Give the position of every malaria parasite, noting whether each is a trophozoite, schizont, or gametocyte.
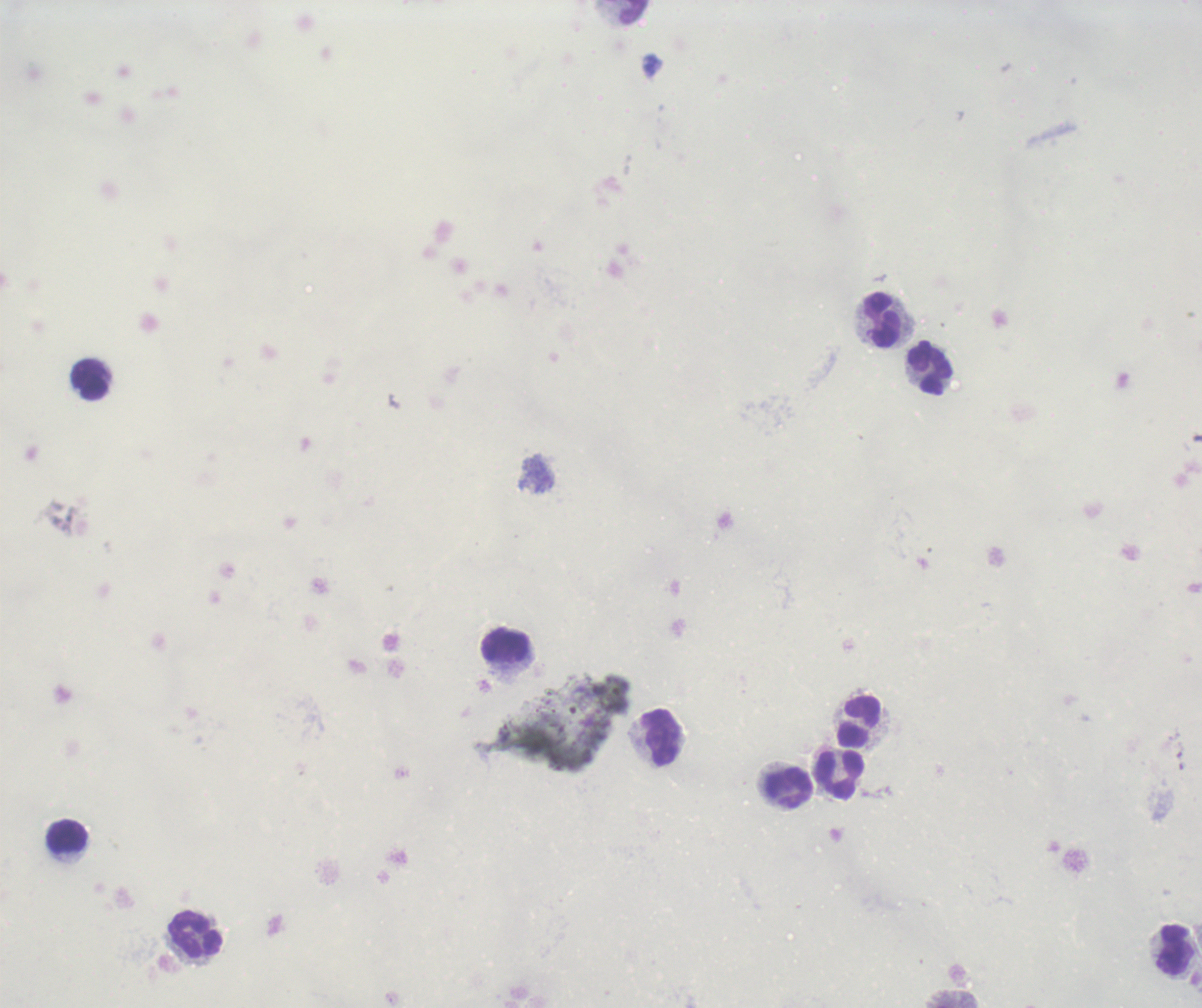

Negative for malaria parasites.

Approximate centers as (x, y) in pixels.
Summary:
  - Leukocyte locations: (634, 12), (883, 321), (931, 369), (91, 379), (506, 646), (859, 721), (662, 738), (840, 774), (788, 788), (68, 837), (196, 934), (1175, 951)
  - Background quality: unsatisfactory
  - Field of view: one from this slide
  - Image size: 1202×1008 pixels
  - Context: previously used in an actual diagnosis
  - Preparation: thick blood film
  - Magnification: 100x
  - Stain: Romanowsky